Report the malaria status of this cell.
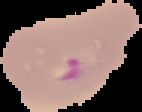
Parasitized.

Image is 142×112 pixels. Segmented cell region on a black background. From a thin blood smear.